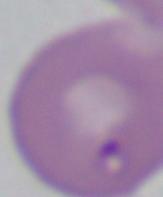
Summary:
  - Identification: Babesia
  - Magnification: 1000x
  - Modality: micrograph